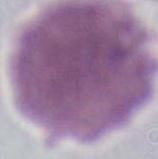

magnification = 1000x
modality = photomicrograph
identification = red blood cell